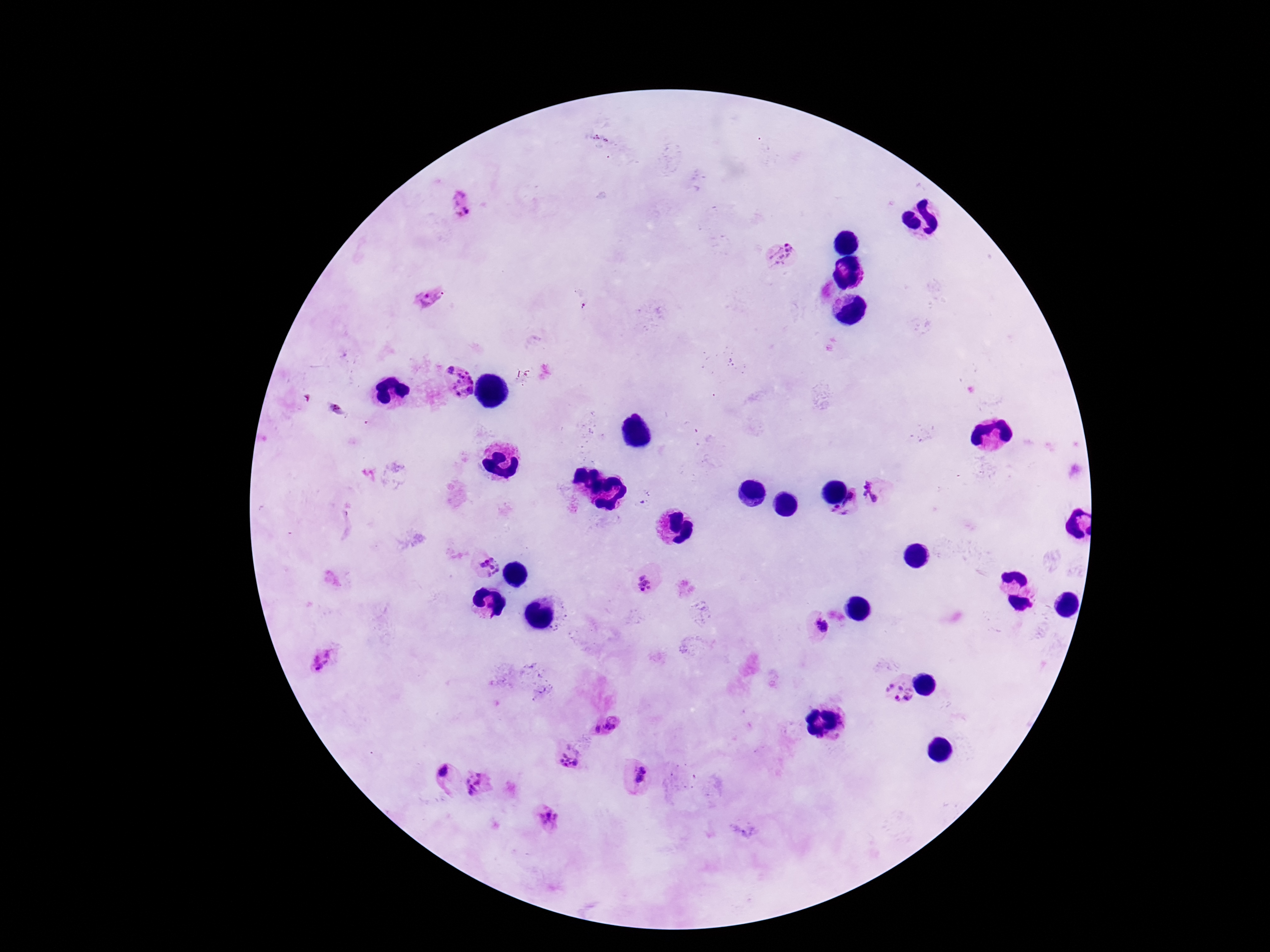

image size = 1270×952 pixels
capture = smartphone camera through the microscope eyepiece
field of view = single
magnification = 100x
preparation = thick peripheral-blood smear
Plasmodium parasite locations = approximate centers as {x, y} in pixels: {460, 205}, {782, 254}, {429, 298}, {448, 368}, {463, 384}, {335, 409}, {875, 491}, {845, 503}, {488, 567}, {645, 584}, {821, 625}, {325, 661}, {899, 692}, {612, 723}, {597, 729}, {570, 758}, {443, 773}, {640, 774}, {478, 785}, {546, 818}
patient malaria status = infected
stain = Giemsa